Assess the morphology of the erythrocytes.
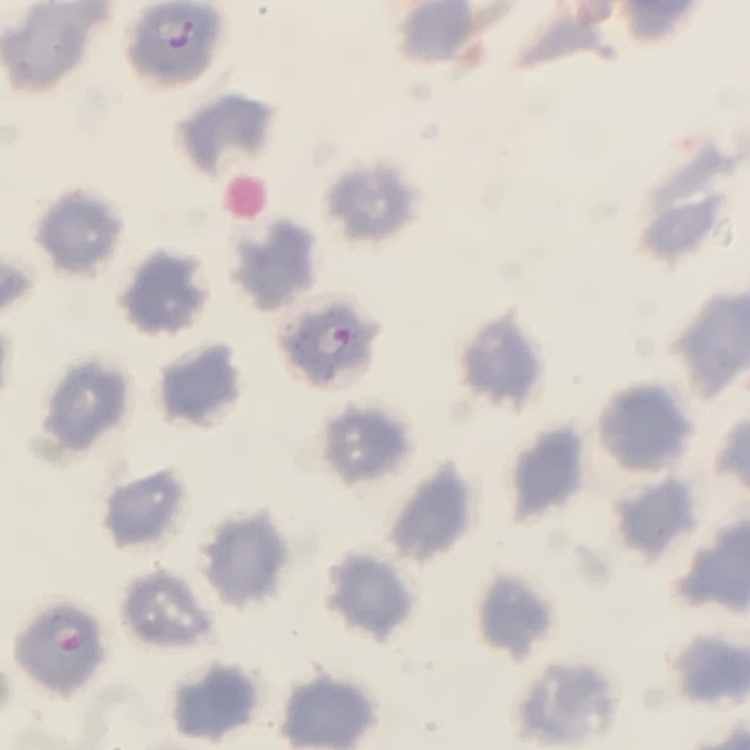
No rouleaux formation.

Square crop of a larger photomicrograph. Thin peripheral smear. Stained with either Field's or Giemsa.